Outline each blood parasite and name the species.
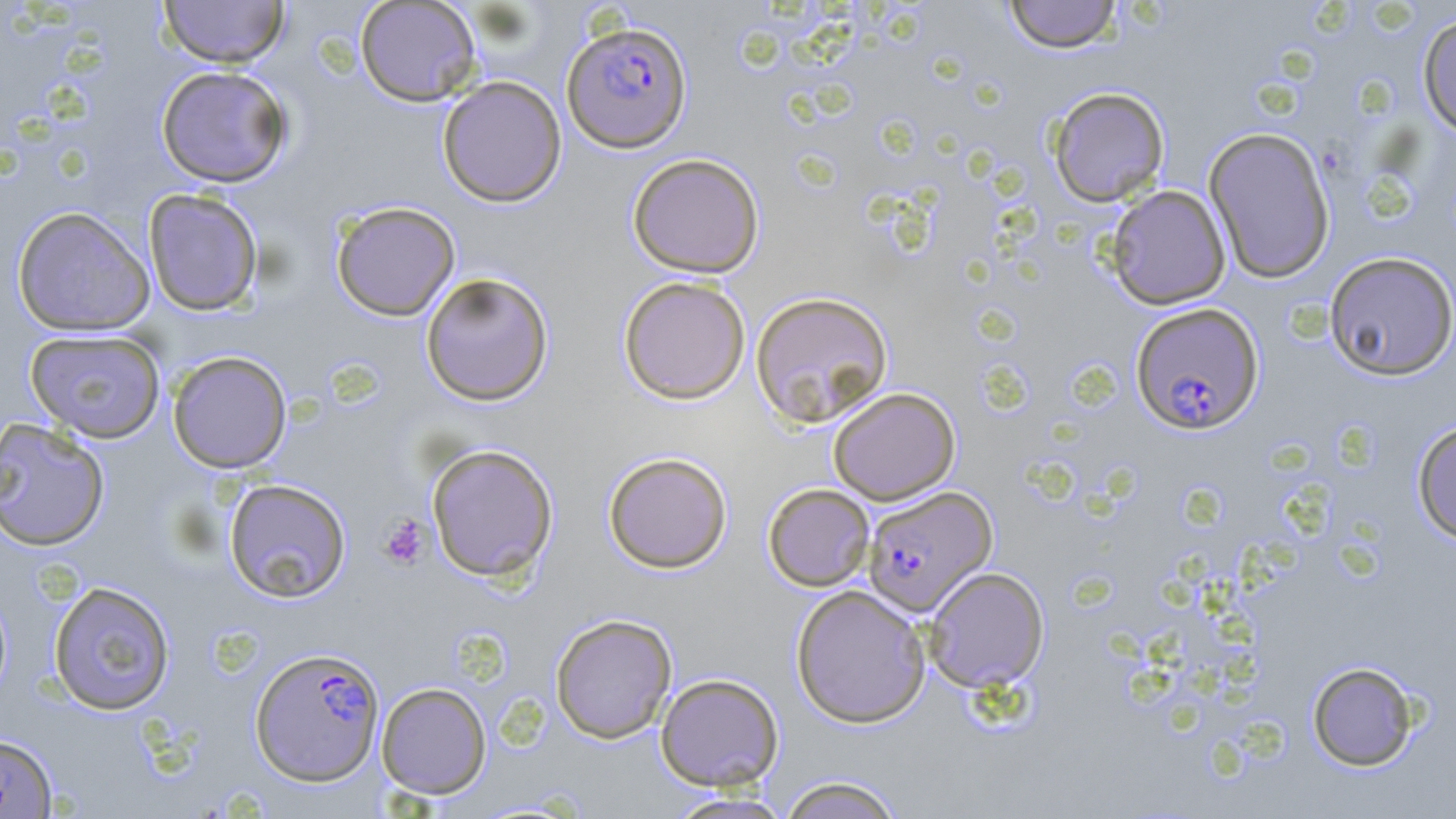

Approximate bounding boxes as (x1, y1, x2, y2) in pixels.
Plasmodium falciparum-infected red blood cells: (562, 20, 693, 153), (1130, 302, 1264, 435), (861, 485, 998, 617), (249, 646, 385, 786).
No Plasmodium ovale, Plasmodium malariae, Plasmodium vivax, Babesia divergens, or Trypanosoma brucei observed.

slide-level diagnosis = Plasmodium falciparum
modality = optical microscopy
uninfected red blood cell locations = approximate bounding boxes as (x1, y1, x2, y2) in pixels: (158, 0, 289, 68), (1003, 0, 1124, 53), (354, 1, 482, 106), (1417, 11, 1456, 139), (155, 65, 293, 188), (437, 75, 567, 207), (1047, 86, 1170, 207), (1202, 126, 1336, 284), (627, 152, 765, 278), (1106, 184, 1231, 310), (143, 188, 264, 315), (330, 200, 461, 321), (12, 206, 155, 336), (1324, 251, 1456, 381), (420, 272, 554, 406), (618, 276, 750, 404), (750, 290, 894, 427), (25, 329, 166, 443), (168, 350, 292, 473), (828, 386, 961, 505), (0, 417, 110, 551), (1412, 420, 1456, 545), (426, 443, 559, 583), (603, 451, 732, 572), (223, 478, 352, 603), (763, 483, 875, 591), (924, 566, 1049, 692), (47, 580, 176, 715), (790, 584, 931, 728), (550, 613, 678, 744), (1307, 661, 1420, 771), (655, 672, 784, 791), (376, 682, 492, 799), (0, 731, 58, 819), (775, 774, 906, 819), (664, 792, 795, 819)
stain = May-Grünwald-Giemsa
field of view = one of a larger specimen
preparation = thin blood film
image size = 1456×819 pixels
magnification = 1000x
platelet locations = approximate bounding boxes as (x1, y1, x2, y2) in pixels: (378, 515, 430, 570)